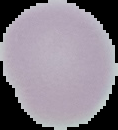

Summary:
  - Result: no Plasmodium parasites seen
  - Image size: 118×130 pixels
  - Image type: segmented cell region with the area outside set to black
  - Preparation: thin blood film